Identify the preparation type.
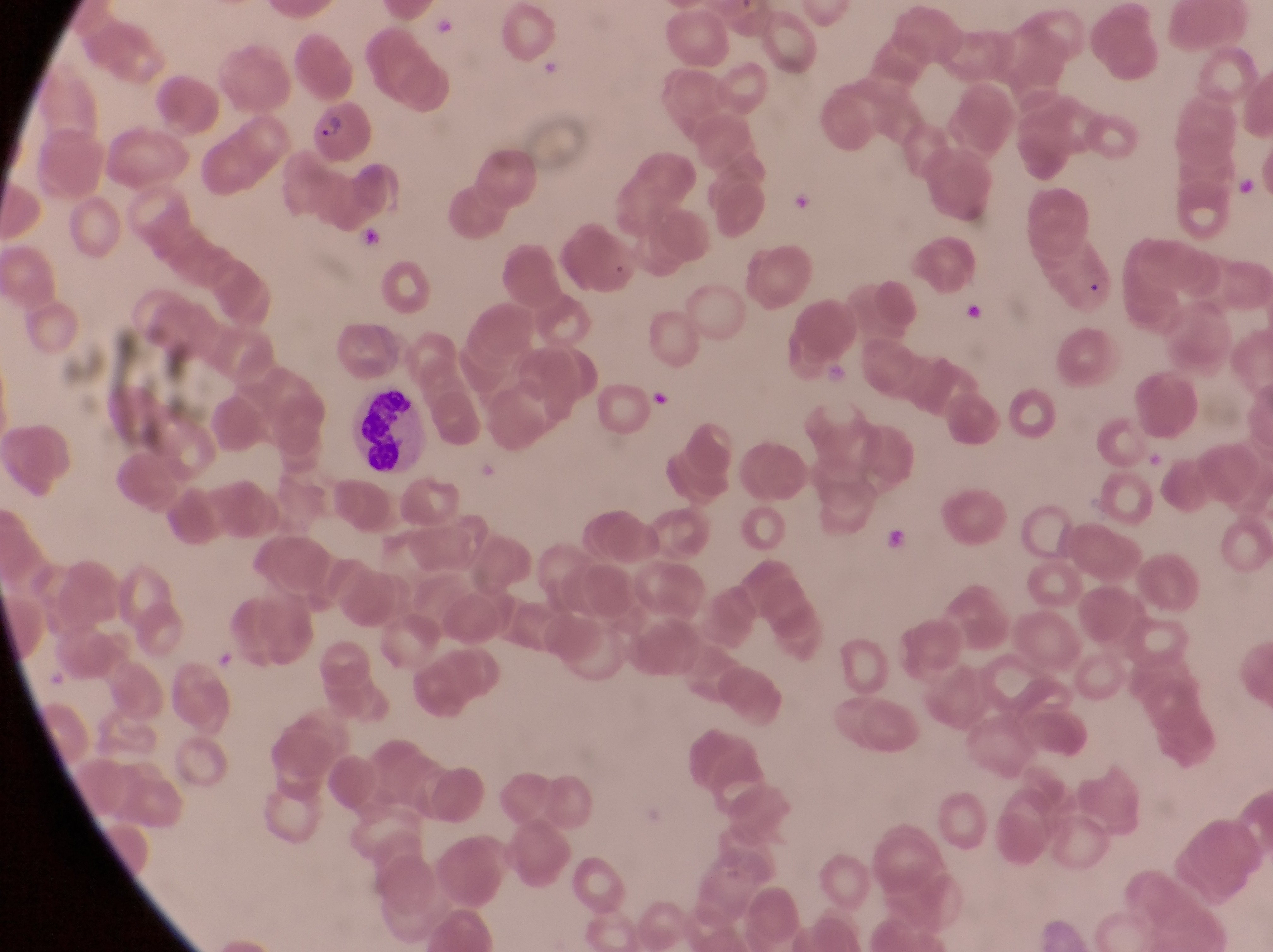
Thin blood smear.

Approximate bounding boxes as {left, top, right, bottom} in pixels.
Summary:
  - Leukocyte locations: {351, 380, 421, 479}
  - Parasitised red blood cell locations: {310, 100, 373, 168}, {350, 217, 389, 259}, {958, 299, 990, 334}, {651, 385, 679, 418}
  - Artifact (platelet-like body, stain precipitate, or debris) locations: {879, 521, 916, 568}
  - Magnification: 1000x
  - Country: Uganda
  - Field of view: single
  - Capture: smartphone photograph through the eyepiece of an Olympus CX-23 microscope
  - Image size: 1273×952 pixels